Identify the blood parasite species.
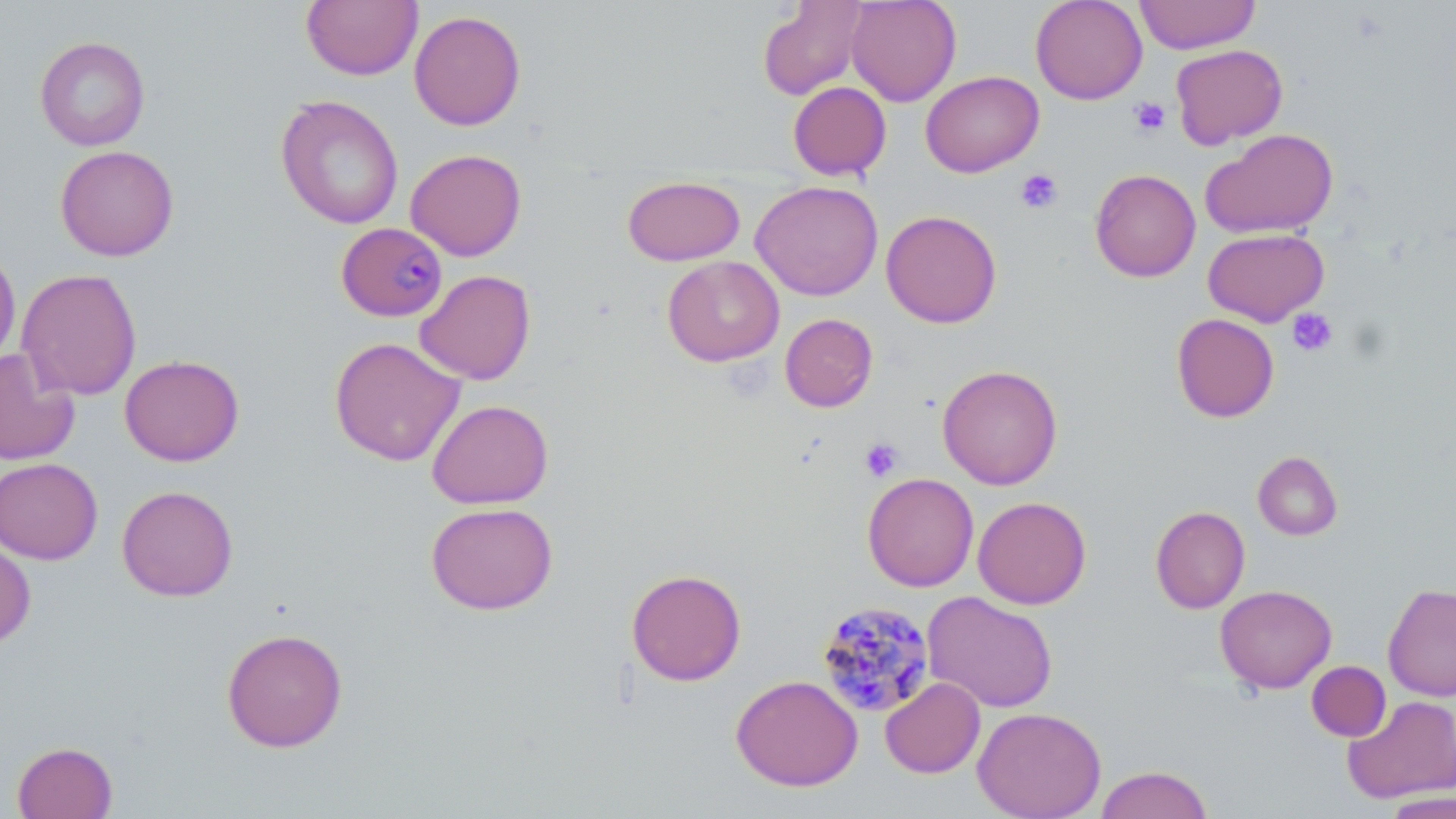
Plasmodium malariae.

Approximate bounding boxes as named x1/y1/x2/y2 corners in pixels. Plasmodium malariae-infected red blood cell locations: (x1=336, y1=222, x2=448, y2=322), (x1=815, y1=601, x2=935, y2=718). Uninfected red blood cell locations: (x1=301, y1=0, x2=422, y2=81), (x1=757, y1=0, x2=868, y2=100), (x1=846, y1=0, x2=962, y2=106), (x1=1030, y1=0, x2=1147, y2=104), (x1=1135, y1=0, x2=1260, y2=54), (x1=409, y1=10, x2=526, y2=131), (x1=34, y1=36, x2=151, y2=151), (x1=1170, y1=43, x2=1288, y2=149), (x1=920, y1=70, x2=1043, y2=177), (x1=788, y1=81, x2=892, y2=181), (x1=275, y1=94, x2=404, y2=230), (x1=1201, y1=128, x2=1339, y2=239), (x1=55, y1=145, x2=179, y2=261), (x1=406, y1=148, x2=527, y2=261), (x1=1090, y1=169, x2=1201, y2=282), (x1=622, y1=175, x2=745, y2=266), (x1=750, y1=180, x2=883, y2=301), (x1=881, y1=210, x2=1002, y2=328), (x1=1203, y1=228, x2=1329, y2=327), (x1=0, y1=244, x2=21, y2=369), (x1=662, y1=256, x2=785, y2=366), (x1=16, y1=268, x2=142, y2=400), (x1=414, y1=269, x2=536, y2=385), (x1=780, y1=313, x2=878, y2=412), (x1=1171, y1=313, x2=1280, y2=423), (x1=329, y1=337, x2=466, y2=466), (x1=0, y1=348, x2=81, y2=465), (x1=120, y1=354, x2=244, y2=466), (x1=937, y1=364, x2=1063, y2=490), (x1=427, y1=399, x2=554, y2=509), (x1=1253, y1=451, x2=1343, y2=540), (x1=0, y1=458, x2=103, y2=564), (x1=862, y1=472, x2=979, y2=591), (x1=116, y1=485, x2=238, y2=601), (x1=972, y1=496, x2=1092, y2=609), (x1=425, y1=502, x2=558, y2=615), (x1=1150, y1=506, x2=1250, y2=614), (x1=0, y1=539, x2=36, y2=650), (x1=626, y1=568, x2=747, y2=686), (x1=1382, y1=583, x2=1456, y2=702), (x1=1215, y1=584, x2=1337, y2=693), (x1=922, y1=591, x2=1058, y2=713), (x1=221, y1=627, x2=348, y2=753), (x1=1307, y1=661, x2=1391, y2=741), (x1=731, y1=674, x2=863, y2=791), (x1=880, y1=677, x2=985, y2=779), (x1=1342, y1=694, x2=1456, y2=804), (x1=973, y1=707, x2=1106, y2=818), (x1=12, y1=741, x2=118, y2=819), (x1=1094, y1=765, x2=1214, y2=819), (x1=1381, y1=791, x2=1456, y2=818). Platelet locations: (x1=1129, y1=96, x2=1171, y2=138), (x1=1015, y1=168, x2=1064, y2=215), (x1=1287, y1=308, x2=1338, y2=358), (x1=859, y1=438, x2=903, y2=482). Light microscopy. Thin blood film. Captured at 1000x magnification. One field of a larger specimen. May-Grünwald-Giemsa stain. Image is 1456×819 pixels.